Identify the preparation type.
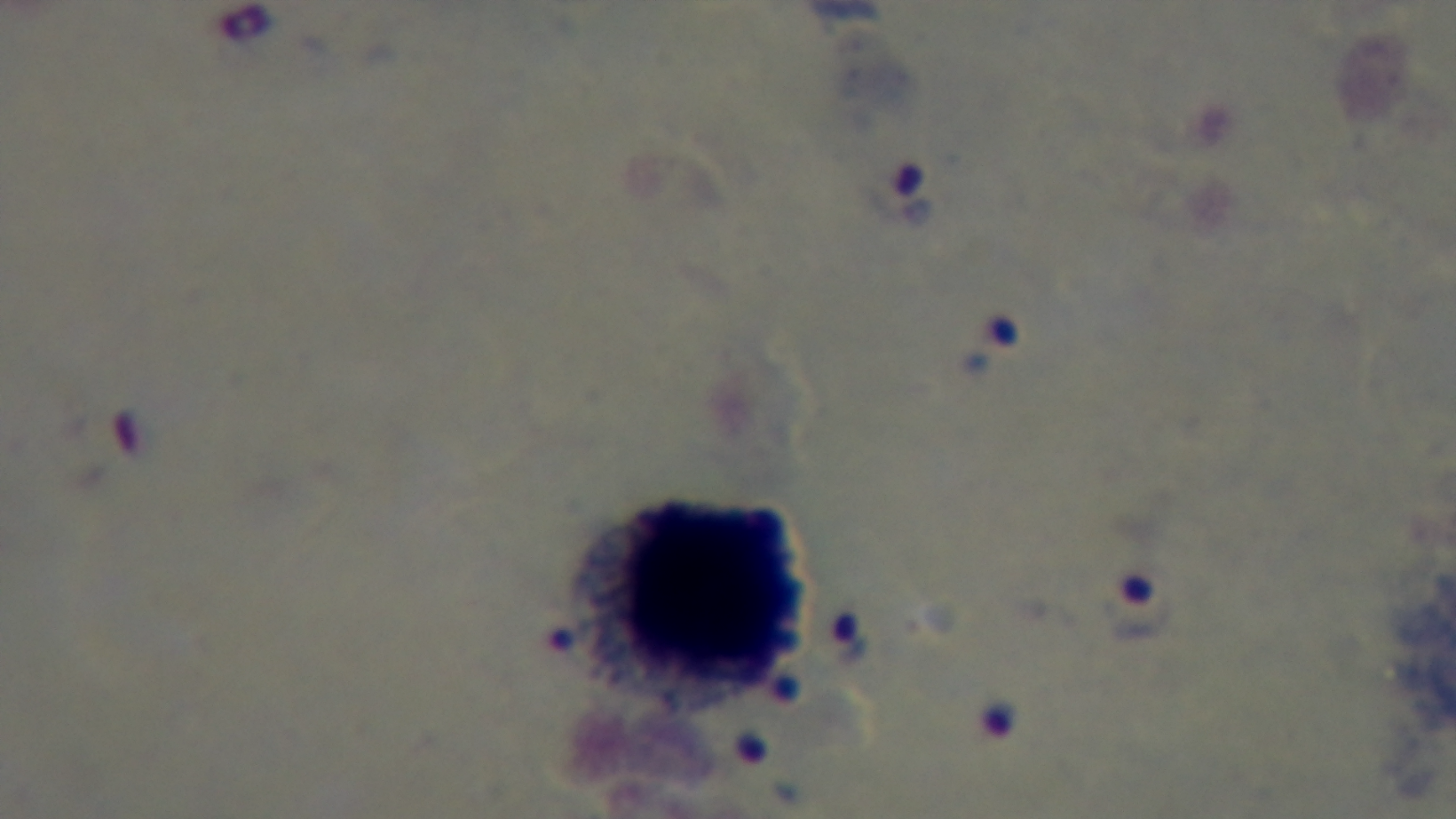
Thick.

Mounted 4K digital camera. 100x oil-immersion objective. One field from the slide. Malaria status: positive. Photomicrograph. Giemsa stain.